Describe the morphology of the erythrocytes.
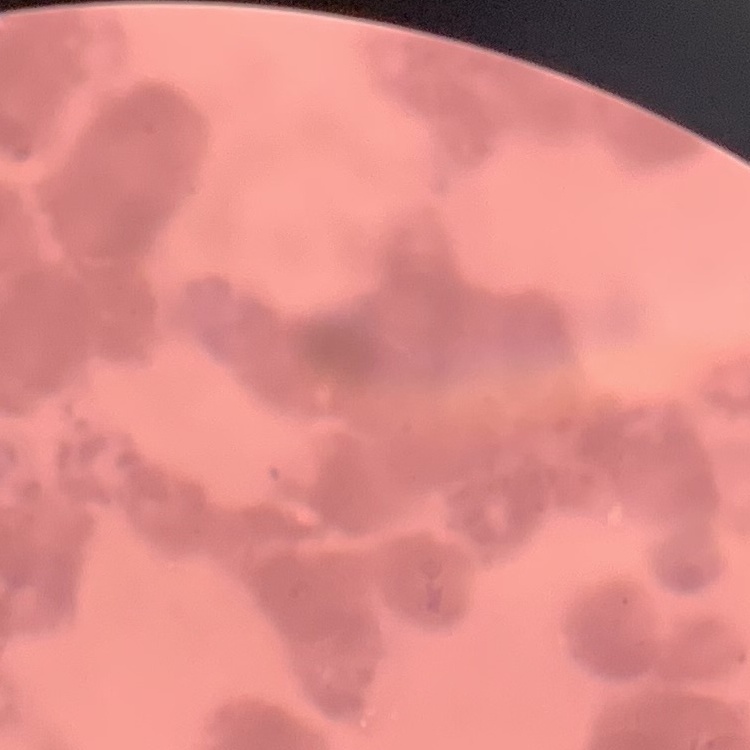
They show rouleaux formation.

Summary:
  - Preparation: thin blood film
  - Image type: square crop of a larger photomicrograph
  - Stain: Field's or Giemsa